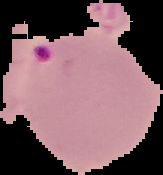
Segmented cell region on a black background. Image is 163×175 pixels. Malaria status: parasitized. From a thin blood film.